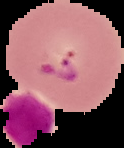
image size = 124×148 pixels
malaria status = parasitized
preparation = thin blood film
image type = segmented cell region on a black background